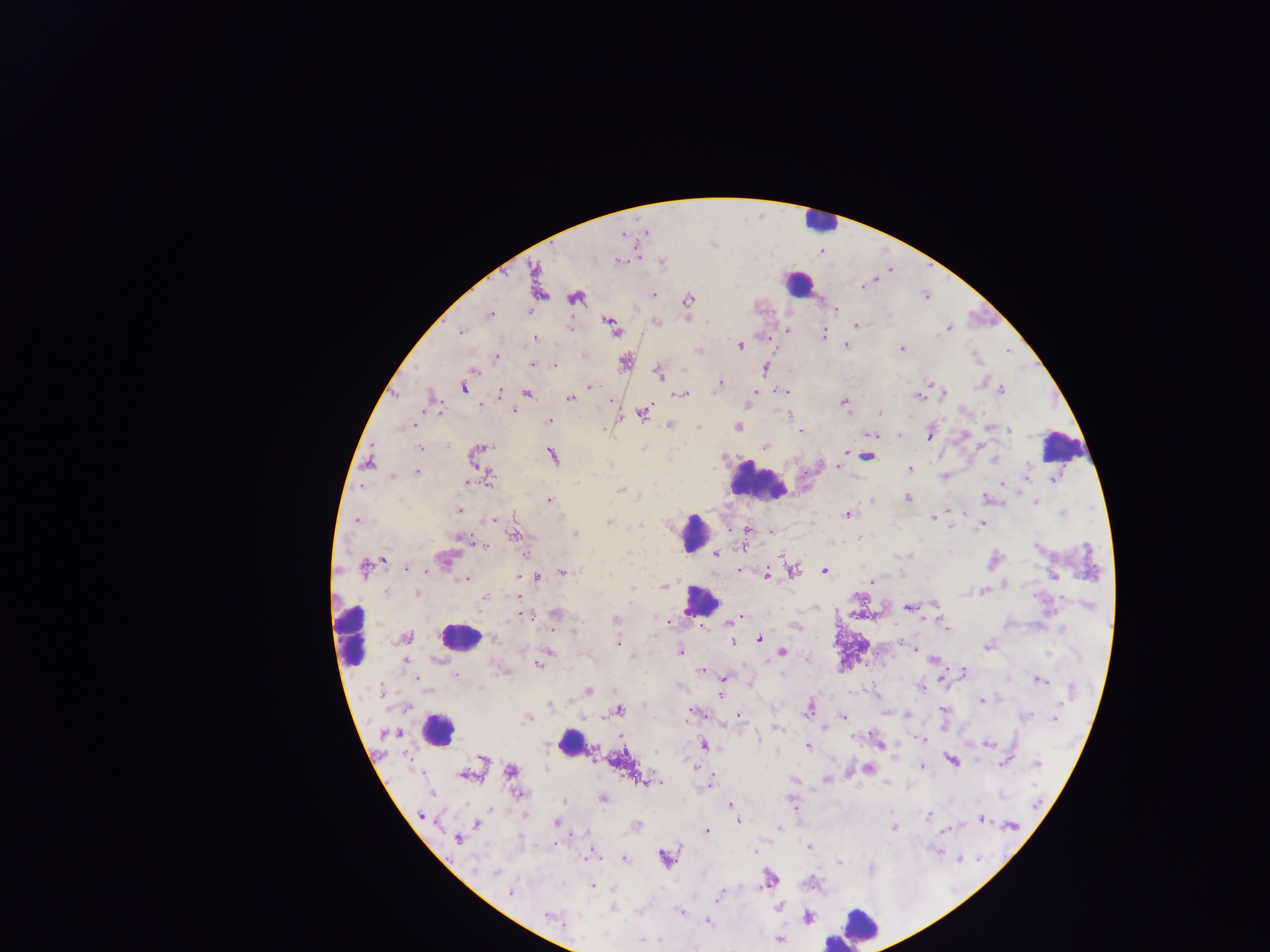
leukocyte locations = approximate centers as (x, y) in pixels: (818, 222), (796, 283), (1060, 444), (758, 482), (694, 532), (701, 601), (459, 636), (351, 638), (438, 730), (570, 742), (861, 925)
country = Ghana
field of view = single
capture = mobile-phone photograph through a microscope
Plasmodium parasite locations = approximate centers as (x, y) in pixels: (618, 261), (535, 277), (864, 285), (653, 295), (576, 298), (687, 300), (835, 309), (529, 310), (489, 315), (655, 322), (857, 325), (613, 327), (569, 328), (787, 329), (947, 329), (461, 331), (823, 334), (535, 338), (845, 345), (740, 346), (902, 349), (699, 350), (496, 356), (625, 362), (533, 364), (554, 366), (765, 368), (474, 370), (659, 373), (720, 382), (979, 384), (463, 387), (590, 387), (784, 390), (1001, 390), (500, 393), (527, 393), (944, 394), (683, 395), (753, 395), (918, 396), (570, 398), (844, 403), (749, 404), (514, 410), (880, 413), (642, 414), (788, 415), (549, 420), (413, 424), (669, 426), (987, 427), (737, 428), (1010, 430), (801, 431), (930, 434), (872, 435), (899, 435), (447, 445), (766, 445), (420, 447), (481, 448), (553, 456), (866, 456), (369, 463), (839, 463), (610, 464), (910, 468), (416, 472), (392, 476), (944, 476), (1027, 476), (490, 478), (1053, 479), (468, 481), (1003, 484), (621, 490), (985, 497), (908, 498), (548, 500), (872, 502), (1036, 502), (460, 509), (1062, 513), (848, 514), (933, 518), (493, 520), (357, 521), (608, 523), (981, 524), (641, 525), (949, 526), (747, 531), (514, 534), (574, 534), (459, 537), (860, 537), (476, 543), (482, 546), (716, 555), (782, 555), (443, 560), (384, 561), (364, 567), (408, 568), (741, 570), (793, 571), (562, 572), (825, 572), (767, 573), (1052, 575), (519, 577), (535, 578), (465, 579), (872, 580), (663, 586), (385, 591), (984, 591), (416, 594), (484, 596), (517, 597), (1090, 606), (908, 608), (555, 613), (530, 615), (738, 618), (615, 619), (660, 619), (668, 621), (729, 622), (796, 627), (947, 629), (1062, 629), (575, 632), (407, 637), (495, 640), (760, 640), (618, 642), (733, 642), (987, 646), (914, 649), (550, 651), (680, 652), (782, 652), (1049, 654), (632, 657), (544, 659), (934, 660), (405, 661), (538, 665), (501, 670), (701, 671), (964, 671), (455, 675), (723, 679), (943, 679), (418, 680), (1040, 680), (922, 688), (381, 690), (1071, 690), (589, 691), (721, 696), (981, 700), (1063, 701), (550, 706), (809, 709), (943, 710), (618, 711), (694, 712), (738, 716), (844, 716), (907, 716), (1026, 717), (527, 718), (1055, 718), (776, 729), (390, 733), (758, 739), (920, 739), (879, 744), (704, 745), (988, 745), (807, 746), (484, 761), (952, 761), (1004, 762), (695, 764), (1037, 764), (922, 767), (511, 770), (868, 770), (464, 776), (794, 780), (647, 781), (657, 781), (826, 781), (710, 783), (433, 793), (520, 793), (603, 799), (563, 801), (793, 803), (730, 806), (420, 814), (929, 815), (982, 819), (738, 821), (556, 823), (476, 824), (636, 826), (1012, 826), (780, 827), (893, 827), (706, 831), (943, 831), (457, 839), (809, 846), (754, 852), (938, 852), (592, 855), (666, 858), (625, 859), (958, 859), (838, 862), (495, 872), (769, 879), (593, 886), (510, 893), (719, 896), (778, 906), (613, 908), (680, 912), (549, 917), (807, 918), (708, 922), (582, 938), (642, 940), (779, 940)
image size = 1270×952 pixels
preparation = thick blood smear